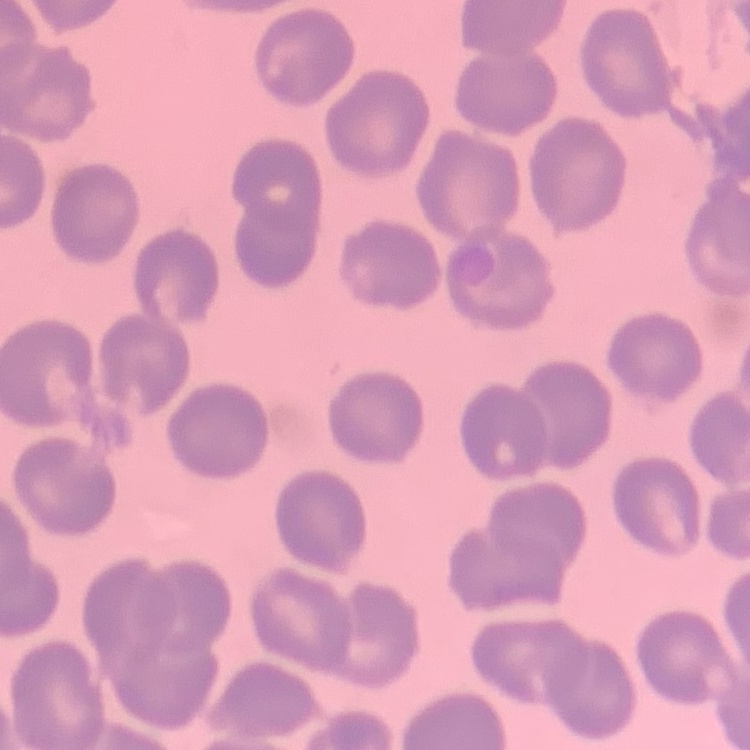

Summary:
  - Red blood cell morphology: no rouleaux formation
  - Image type: square crop of a larger photomicrograph
  - Preparation: thin peripheral smear
  - Stain: Field's or Giemsa